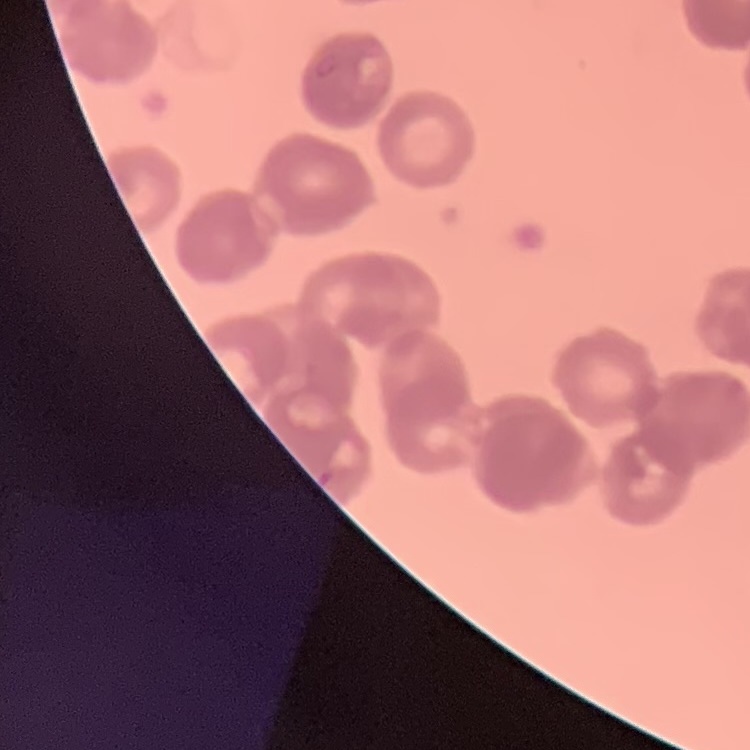

{
  "red_blood_cell_morphology": "rouleaux formation",
  "image_type": "one tile cut from a larger photomicrograph",
  "stain": "Field's or Giemsa",
  "preparation": "thin peripheral smear"
}